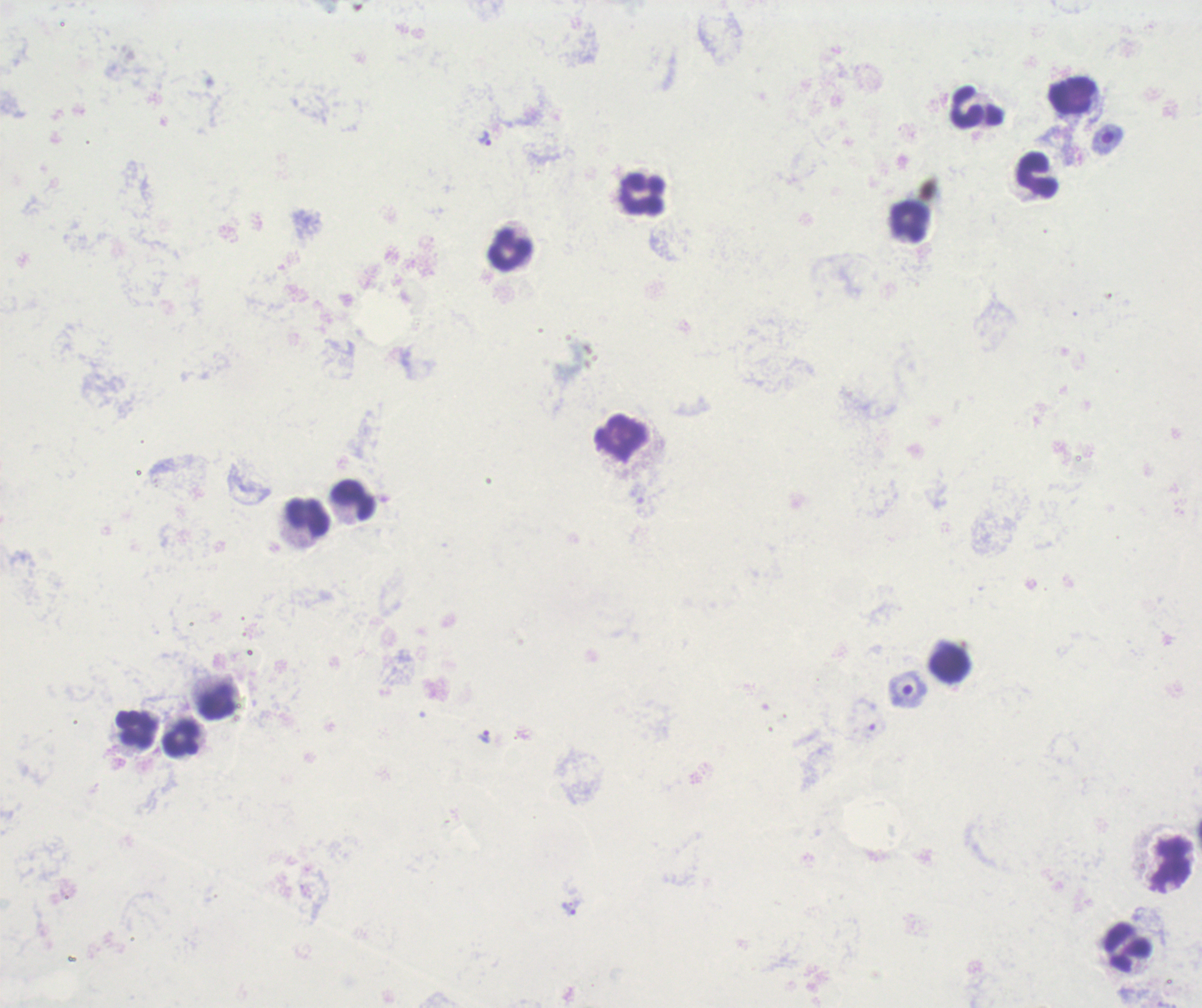

Approximate centers as {x, y} in pixels.
Summary:
  - Leukocyte locations: {1074, 96}, {967, 108}, {1038, 175}, {645, 195}, {910, 223}, {510, 250}, {622, 441}, {352, 501}, {308, 517}, {951, 663}, {214, 701}, {135, 728}, {182, 740}, {1171, 864}, {1127, 949}
  - Trophozoite locations: {483, 137}, {483, 736}, {569, 907}
  - Field of view: one from this slide
  - Background quality: unsatisfactory
  - Preparation: thick blood smear
  - Context: previously used in an actual diagnosis
  - Image size: 1202×1008 pixels
  - Result: positive for malaria parasites
  - Stain: Romanowsky
  - Magnification: 100x